Locate every Plasmodium falciparum-infected red blood cell.
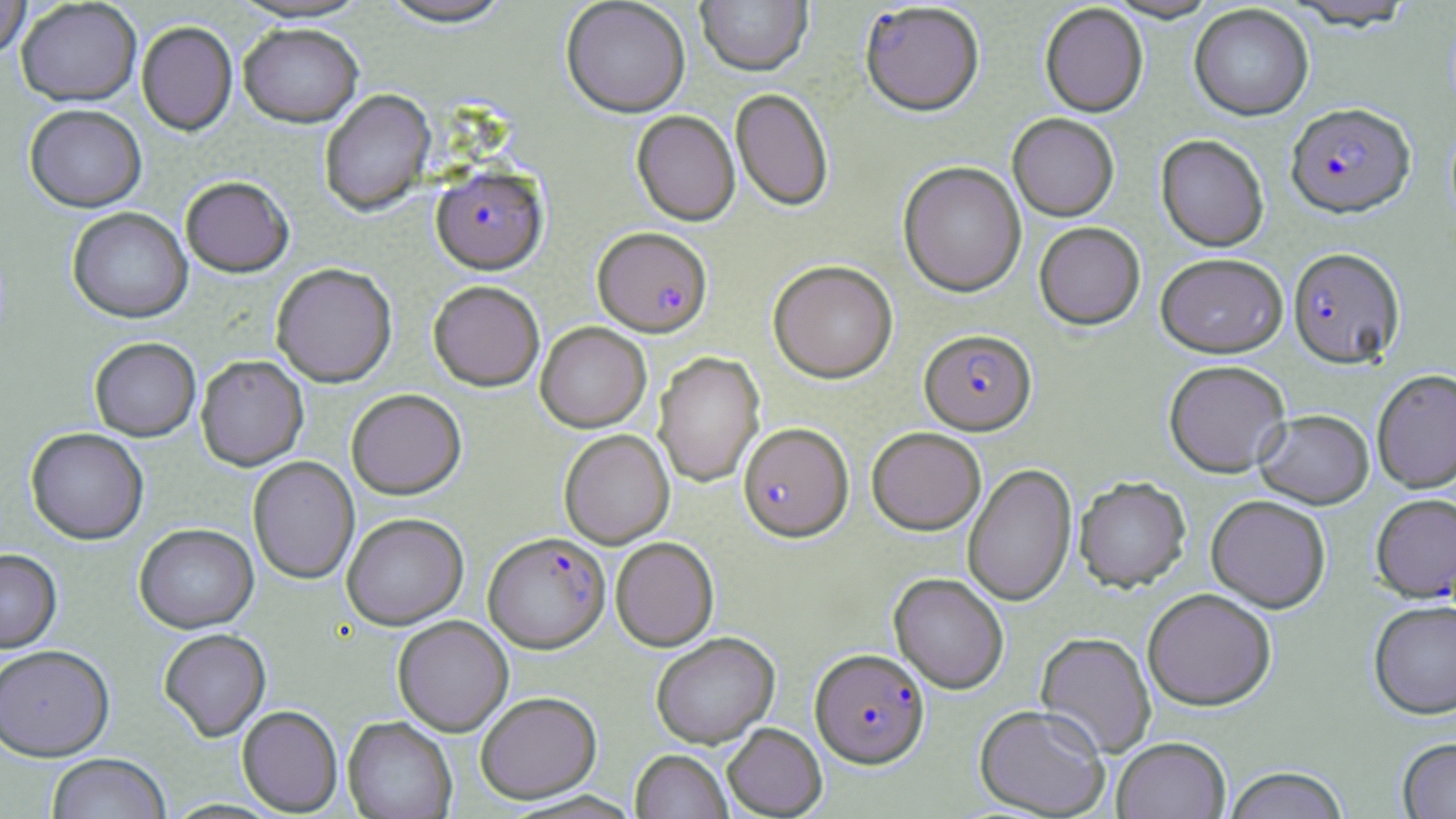

Approximate bounding boxes as (x1, y1, x2, y2) in pixels.
Plasmodium falciparum-infected red blood cells: (860, 3, 984, 117), (1286, 104, 1415, 219), (431, 165, 547, 274), (593, 227, 713, 337), (1288, 249, 1405, 370), (919, 330, 1037, 435), (738, 423, 854, 542), (1371, 494, 1456, 603), (484, 532, 610, 652), (810, 648, 930, 769).

slide-level diagnosis = Plasmodium falciparum
stain = May-Grünwald-Giemsa
magnification = 1000x
preparation = thin blood smear
field of view = single
image size = 1456×819 pixels
modality = optical microscopy
uninfected red blood cell locations = approximate bounding boxes as (x1, y1, x2, y2) in pixels: (0, 0, 31, 59), (16, 0, 142, 105), (376, 0, 517, 27), (561, 0, 690, 117), (696, 0, 812, 76), (1103, 0, 1222, 23), (1283, 1, 1418, 32), (1039, 4, 1148, 117), (1189, 5, 1314, 121), (136, 21, 237, 135), (238, 23, 363, 127), (319, 89, 435, 216), (731, 89, 834, 211), (24, 104, 146, 212), (631, 111, 740, 225), (1007, 114, 1119, 222), (1155, 135, 1269, 252), (898, 162, 1026, 298), (180, 176, 294, 277), (66, 206, 193, 323), (1034, 222, 1145, 331), (1156, 253, 1287, 358), (768, 260, 898, 384), (271, 263, 397, 387), (428, 280, 545, 391), (535, 322, 651, 432), (89, 337, 201, 440), (652, 351, 765, 487), (195, 355, 308, 470), (1163, 361, 1291, 478), (1372, 369, 1456, 494), (346, 388, 466, 498), (1254, 411, 1374, 511), (25, 427, 149, 544), (867, 427, 985, 535), (559, 430, 674, 548), (247, 456, 359, 584), (963, 463, 1077, 607), (1074, 479, 1191, 593), (1206, 496, 1331, 614), (342, 512, 468, 629), (134, 523, 258, 633), (611, 537, 719, 651), (0, 548, 62, 652), (889, 573, 1009, 694), (1143, 590, 1276, 711), (1368, 602, 1456, 721), (392, 616, 513, 736), (158, 628, 271, 741), (650, 633, 779, 748), (1035, 633, 1156, 759), (0, 644, 114, 761), (475, 691, 601, 803), (974, 704, 1109, 818), (237, 705, 343, 815), (343, 716, 457, 819), (722, 723, 827, 818), (1112, 738, 1230, 819), (1396, 739, 1456, 819), (631, 750, 732, 819), (46, 753, 170, 819), (1224, 767, 1349, 819)